Locate every blood parasite and identify its species.
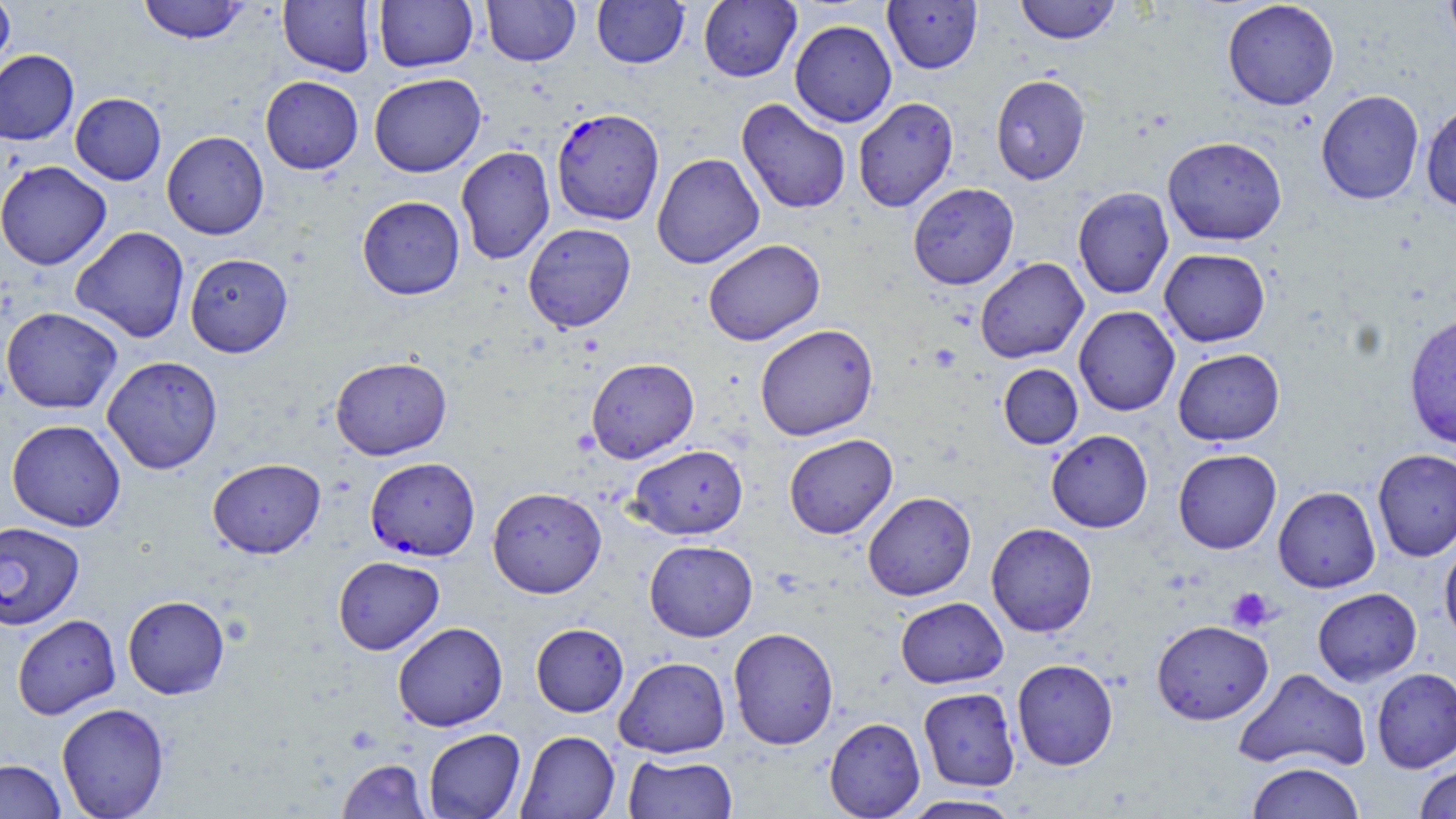
Approximate bounding boxes as [x1, y1, x2, y2] in pixels.
Plasmodium falciparum-infected red blood cells: [551, 107, 664, 225], [365, 457, 480, 560], [0, 522, 85, 630].
No Plasmodium ovale, Plasmodium malariae, Plasmodium vivax, Babesia divergens, or Trypanosoma brucei observed.

Uninfected red blood cell locations: [0, 0, 15, 80], [137, 0, 250, 44], [278, 0, 376, 76], [373, 0, 478, 73], [482, 0, 580, 66], [592, 0, 690, 69], [697, 0, 802, 82], [1015, 0, 1121, 44], [1222, 0, 1339, 110], [1443, 0, 1456, 55], [883, 1, 983, 74], [789, 19, 897, 127], [0, 49, 79, 145], [369, 73, 486, 177], [990, 74, 1090, 185], [260, 75, 363, 174], [1316, 89, 1424, 205], [70, 92, 166, 185], [853, 97, 959, 212], [736, 98, 851, 215], [1420, 102, 1456, 212], [161, 131, 269, 239], [1162, 136, 1287, 246], [455, 146, 555, 264], [651, 153, 764, 269], [0, 160, 112, 270], [907, 183, 1019, 289], [1072, 186, 1174, 300], [357, 196, 465, 300], [523, 223, 636, 332], [70, 225, 190, 342], [703, 238, 825, 345], [1159, 248, 1270, 347], [184, 252, 293, 357], [975, 257, 1088, 363], [1073, 305, 1180, 416], [1, 307, 123, 414], [1403, 313, 1456, 450], [754, 323, 878, 441], [1173, 348, 1284, 446], [101, 355, 223, 474], [330, 356, 452, 460], [586, 358, 700, 463], [998, 364, 1083, 449], [6, 419, 126, 532], [1046, 430, 1153, 533], [784, 434, 897, 539], [628, 445, 748, 540], [1173, 448, 1281, 554], [1372, 448, 1456, 561], [207, 457, 326, 559], [1273, 486, 1381, 593], [487, 487, 606, 598], [862, 492, 976, 600], [985, 522, 1097, 637], [644, 540, 758, 641], [1440, 542, 1456, 649], [333, 556, 444, 655], [1312, 587, 1422, 686], [122, 594, 230, 699], [895, 597, 1008, 688], [12, 614, 121, 719], [1151, 619, 1273, 725], [392, 621, 508, 732], [531, 623, 628, 717], [728, 627, 839, 750], [614, 656, 731, 758], [1011, 658, 1118, 770], [1371, 667, 1456, 772], [1234, 668, 1371, 773], [918, 687, 1021, 792], [56, 702, 170, 819], [824, 717, 925, 818], [424, 728, 525, 818], [516, 730, 620, 819], [623, 753, 738, 818], [337, 758, 431, 819], [0, 759, 67, 819], [1245, 761, 1365, 819], [1413, 764, 1456, 819], [897, 794, 1026, 818]. Platelet locations: [928, 344, 961, 372], [1226, 586, 1277, 633]. Slide-level diagnosis: Plasmodium falciparum. Thin blood film. Optical microscopy. Captured at 1000x magnification. May-Grünwald-Giemsa-stained preparation. Image is 1456×819 pixels. Single field of view.